Assess the morphology of the erythrocytes.
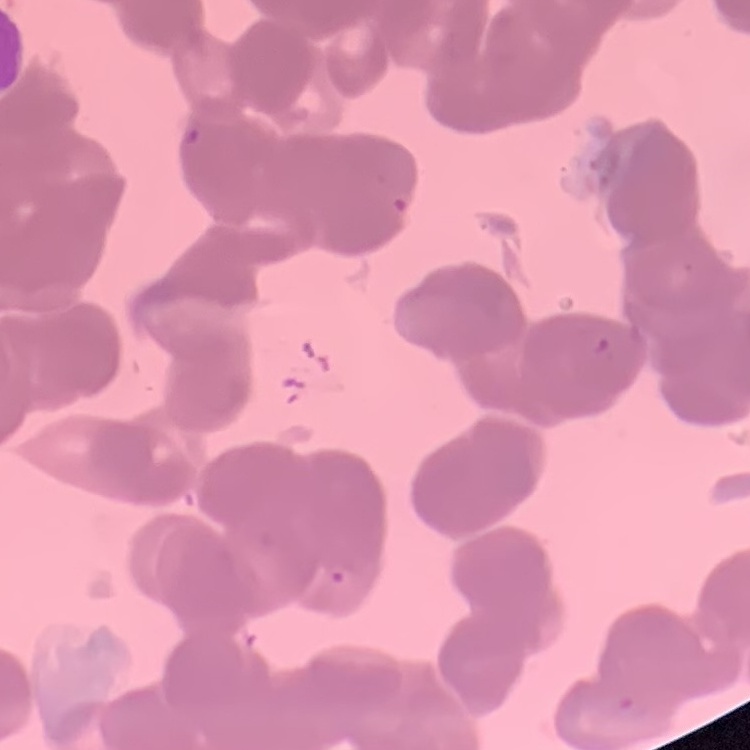
Rouleaux formation.

Summary:
  - Preparation: thin peripheral smear
  - Stain: Field's or Giemsa
  - Image type: square crop of a larger photomicrograph